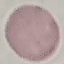 Malaria status: uninfected. Photographed with a smartphone camera at the microscope eyepiece. Cell patch, automatically extracted from a larger field of view and resized to 64 × 64 pixels. Giemsa-stained preparation. Thin smear of blood.